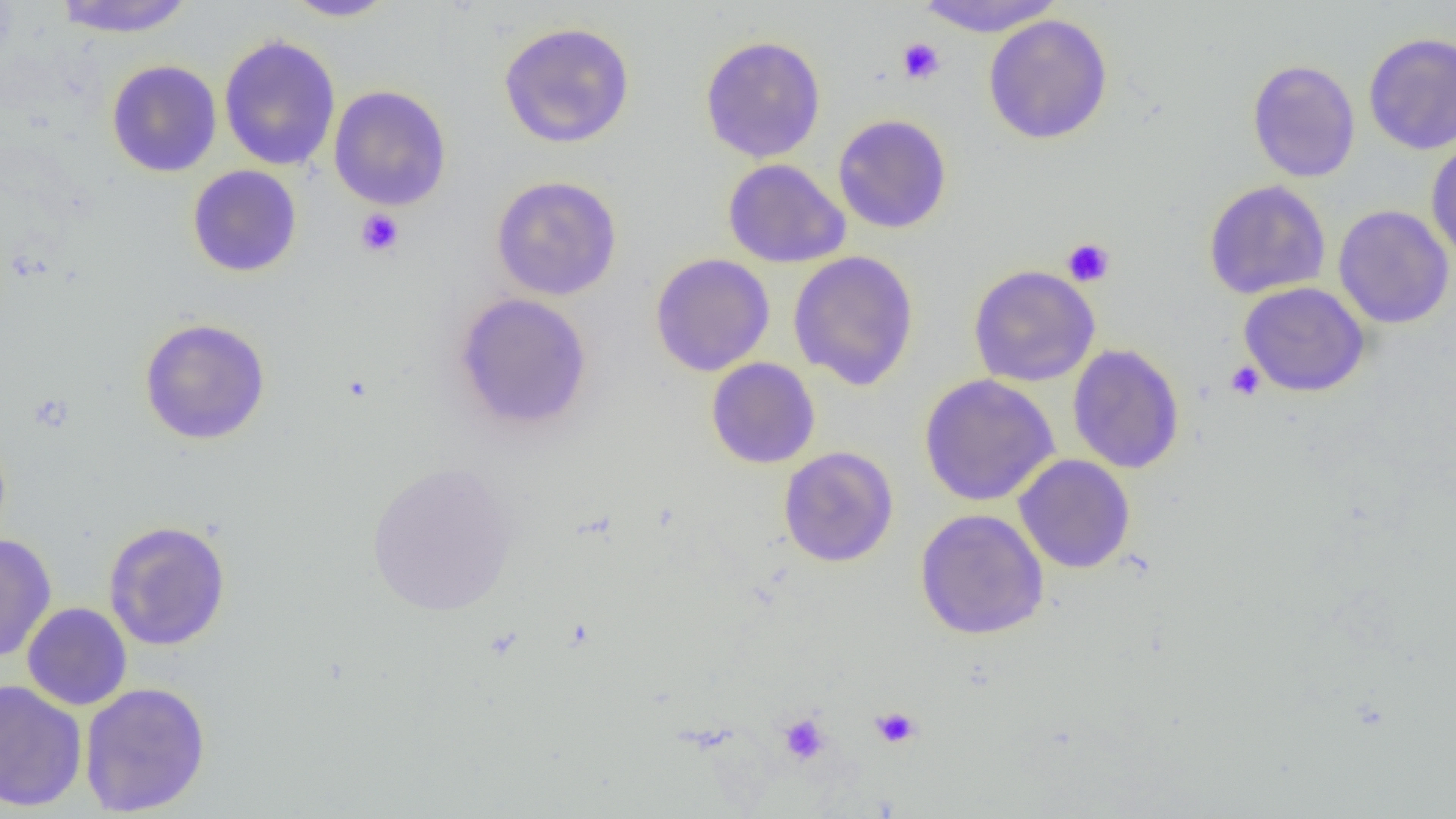
Summary:
  - Coordinate format: approximate bounding boxes as (x1,y1)-(x2,y2) corner pairs in pixels
  - Uninfected red blood cell locations: (52,0)-(197,37), (914,0)-(1066,37), (282,1)-(398,21), (983,14)-(1113,145), (498,20)-(636,148), (1363,32)-(1456,155), (700,34)-(826,163), (218,35)-(341,171), (1246,58)-(1361,182), (106,59)-(223,177), (328,84)-(452,211), (832,114)-(952,234), (1426,138)-(1456,264), (722,158)-(849,268), (187,164)-(303,277), (490,175)-(623,301), (1203,180)-(1331,299), (1333,204)-(1454,329), (788,250)-(919,391), (649,253)-(775,377), (968,265)-(1100,387), (1239,282)-(1370,397), (453,292)-(594,433), (138,317)-(271,445), (1067,343)-(1185,474), (706,357)-(820,469), (918,374)-(1059,506), (778,446)-(899,568), (1014,454)-(1135,574), (366,460)-(519,617), (915,508)-(1049,639), (103,519)-(231,652), (0,533)-(57,663), (22,603)-(132,710), (0,679)-(87,812), (79,682)-(211,817)
  - Platelet locations: (896,37)-(945,85), (355,209)-(404,257), (1061,237)-(1115,287), (1225,361)-(1265,401), (870,706)-(921,749), (777,713)-(830,765)
  - Slide-level diagnosis: no evidence of blood parasites
  - Image size: 1456×819 pixels
  - Modality: light microscopy
  - Preparation: thin blood smear
  - Field of view: single
  - Magnification: 1000x